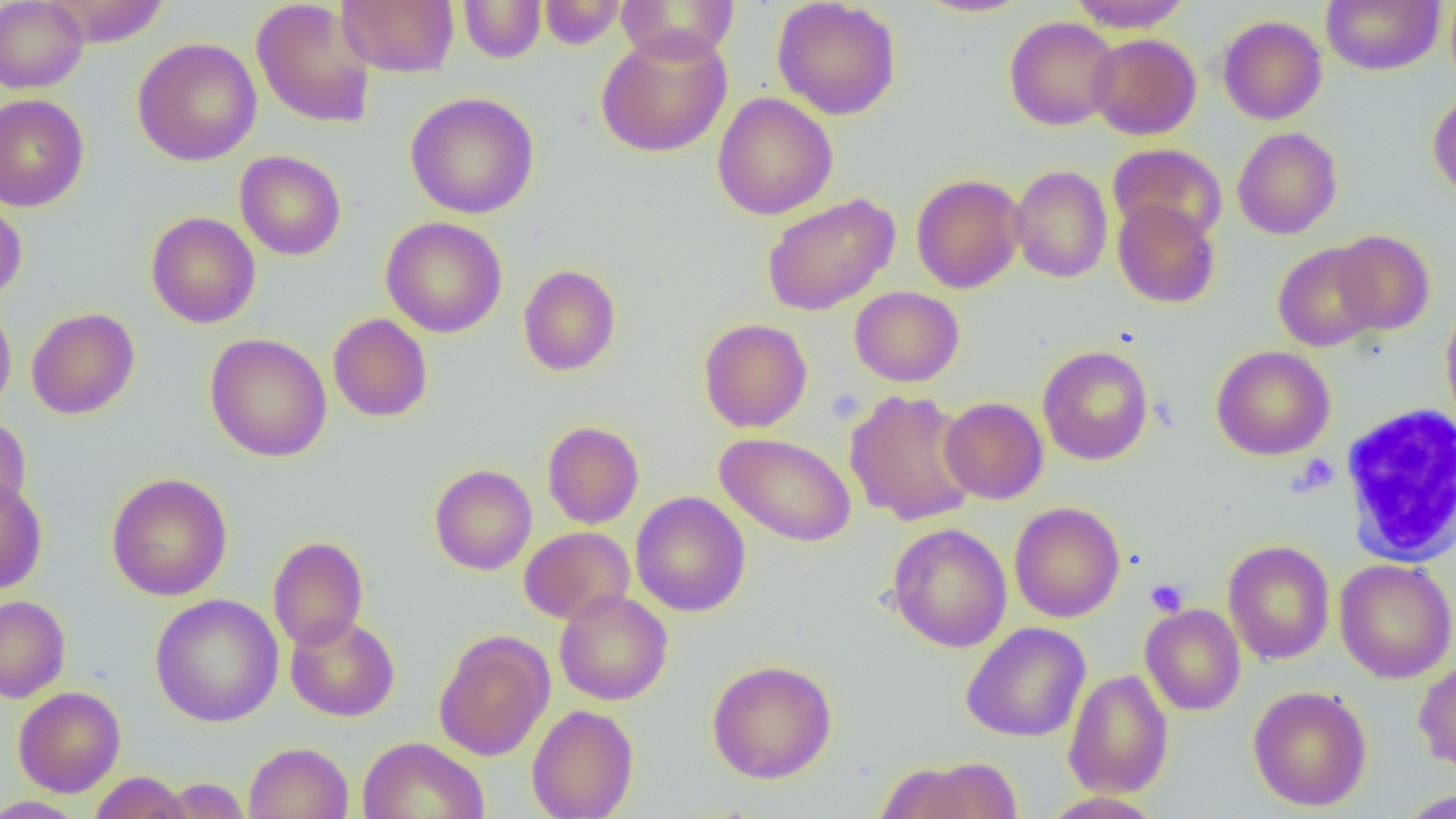

slide_level_diagnosis: no evidence of blood parasites
uninfected_red_blood_cell_locations: 'approximate bounding boxes as named x1/y1/x2/y2 corners in pixels: (x1=0, y1=0, x2=89, y2=93), (x1=42, y1=0, x2=170, y2=47), (x1=251, y1=0, x2=377, y2=129), (x1=337, y1=0, x2=459, y2=77), (x1=771, y1=0, x2=902, y2=121), (x1=913, y1=0, x2=1034, y2=18), (x1=1066, y1=0, x2=1193, y2=32), (x1=1321, y1=0, x2=1445, y2=75), (x1=1445, y1=0, x2=1456, y2=91), (x1=458, y1=1, x2=546, y2=63), (x1=537, y1=1, x2=627, y2=48), (x1=615, y1=1, x2=740, y2=64), (x1=1218, y1=15, x2=1327, y2=125), (x1=1005, y1=16, x2=1121, y2=131), (x1=595, y1=29, x2=733, y2=158), (x1=1087, y1=33, x2=1201, y2=140), (x1=132, y1=37, x2=263, y2=166), (x1=394, y1=91, x2=516, y2=337), (x1=405, y1=91, x2=540, y2=219), (x1=712, y1=92, x2=838, y2=220), (x1=1428, y1=92, x2=1456, y2=203), (x1=0, y1=94, x2=89, y2=212), (x1=1232, y1=127, x2=1343, y2=239), (x1=1108, y1=143, x2=1227, y2=244), (x1=235, y1=150, x2=346, y2=260), (x1=1009, y1=165, x2=1113, y2=283), (x1=911, y1=174, x2=1026, y2=294), (x1=761, y1=193, x2=900, y2=316), (x1=0, y1=197, x2=27, y2=303), (x1=1112, y1=199, x2=1220, y2=309), (x1=145, y1=212, x2=260, y2=328), (x1=380, y1=216, x2=508, y2=338), (x1=1332, y1=230, x2=1436, y2=335), (x1=1273, y1=242, x2=1382, y2=352), (x1=518, y1=264, x2=621, y2=376), (x1=849, y1=286, x2=964, y2=387), (x1=0, y1=298, x2=16, y2=417), (x1=1440, y1=302, x2=1456, y2=429), (x1=26, y1=307, x2=140, y2=419), (x1=328, y1=313, x2=433, y2=422), (x1=698, y1=318, x2=813, y2=432), (x1=204, y1=333, x2=332, y2=462), (x1=1038, y1=345, x2=1153, y2=466), (x1=1211, y1=345, x2=1335, y2=461), (x1=844, y1=389, x2=979, y2=526), (x1=939, y1=396, x2=1049, y2=505), (x1=0, y1=415, x2=31, y2=520), (x1=542, y1=421, x2=644, y2=529), (x1=716, y1=432, x2=856, y2=547), (x1=429, y1=464, x2=537, y2=575), (x1=106, y1=472, x2=233, y2=601), (x1=0, y1=478, x2=47, y2=593), (x1=631, y1=491, x2=751, y2=617), (x1=1009, y1=501, x2=1125, y2=623), (x1=886, y1=523, x2=1012, y2=652), (x1=519, y1=526, x2=635, y2=625), (x1=267, y1=536, x2=369, y2=651), (x1=1222, y1=540, x2=1335, y2=664), (x1=1222, y1=548, x2=1454, y2=670), (x1=1334, y1=559, x2=1456, y2=683), (x1=554, y1=589, x2=673, y2=705), (x1=150, y1=594, x2=283, y2=727), (x1=0, y1=595, x2=71, y2=703), (x1=1140, y1=604, x2=1246, y2=716), (x1=285, y1=614, x2=400, y2=722), (x1=961, y1=622, x2=1090, y2=743), (x1=434, y1=632, x2=554, y2=761), (x1=707, y1=659, x2=837, y2=784), (x1=1413, y1=660, x2=1456, y2=773), (x1=1063, y1=669, x2=1174, y2=798), (x1=1248, y1=685, x2=1372, y2=811), (x1=13, y1=686, x2=126, y2=797), (x1=526, y1=704, x2=638, y2=819), (x1=357, y1=735, x2=489, y2=819), (x1=243, y1=741, x2=354, y2=819), (x1=912, y1=758, x2=1023, y2=819), (x1=88, y1=771, x2=194, y2=819), (x1=159, y1=777, x2=252, y2=818), (x1=1397, y1=788, x2=1456, y2=818), (x1=1041, y1=791, x2=1164, y2=819), (x1=0, y1=795, x2=88, y2=819)'
modality: light microscopy
white_blood_cell_locations: 'approximate bounding boxes as named x1/y1/x2/y2 corners in pixels: (x1=1339, y1=404, x2=1456, y2=567)'
preparation: thin blood film
platelet_locations: 'approximate bounding boxes as named x1/y1/x2/y2 corners in pixels: (x1=827, y1=387, x2=865, y2=424), (x1=1293, y1=453, x2=1339, y2=495), (x1=1145, y1=578, x2=1188, y2=616)'
image_size: 1456×819 pixels
field_of_view: single
magnification: 1000x